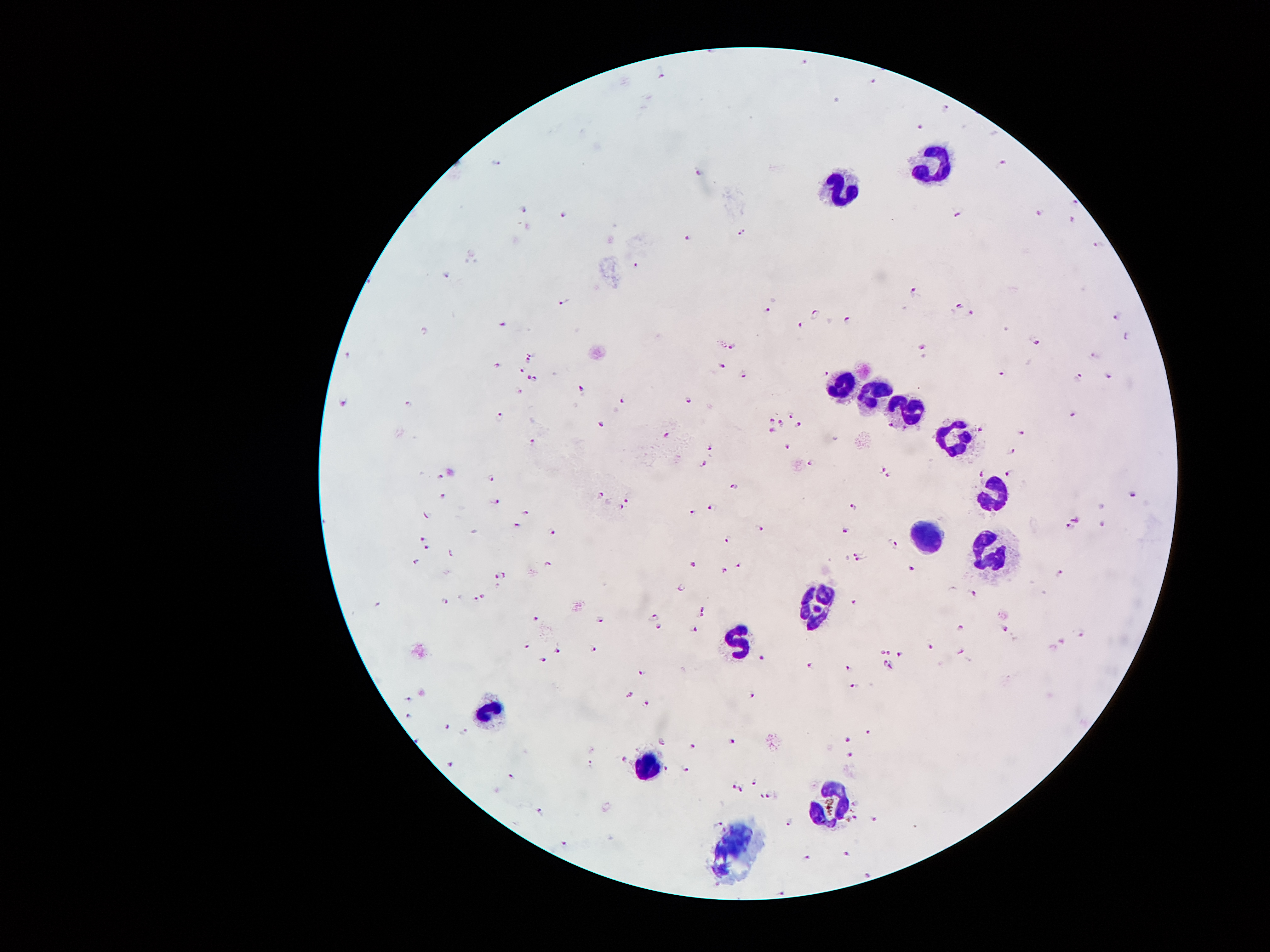
Approximate centers as [x, y] in pixels.
Summary:
  - Plasmodium parasite locations: [803, 60], [663, 76], [874, 82], [838, 98], [946, 109], [919, 126], [1002, 162], [498, 163], [698, 172], [1076, 204], [523, 208], [1038, 213], [560, 214], [957, 219], [1072, 220], [742, 232], [683, 236], [1097, 244], [635, 264], [445, 273], [509, 287], [914, 291], [562, 303], [958, 304], [766, 311], [970, 313], [815, 314], [848, 318], [1119, 318], [503, 324], [802, 325], [424, 329], [1125, 336], [1036, 341], [730, 346], [920, 346], [532, 352], [347, 355], [1096, 357], [529, 362], [494, 366], [723, 366], [522, 370], [827, 371], [1002, 373], [1079, 376], [741, 377], [529, 378], [536, 378], [1109, 378], [581, 388], [519, 390], [621, 399], [344, 401], [687, 401], [409, 403], [789, 413], [1073, 413], [500, 414], [771, 418], [780, 422], [599, 425], [797, 425], [773, 429], [980, 429], [1022, 432], [667, 435], [532, 440], [785, 446], [711, 447], [1014, 450], [701, 462], [810, 463], [882, 470], [981, 472], [438, 474], [1008, 474], [890, 476], [489, 477], [735, 485], [600, 493], [1134, 493], [442, 496], [495, 499], [626, 501], [713, 505], [620, 508], [853, 508], [691, 512], [526, 513], [427, 516], [1074, 517], [517, 524], [760, 525], [1102, 525], [1069, 528], [846, 529], [550, 530], [423, 537], [730, 539], [897, 543], [428, 546], [856, 550], [450, 554], [416, 562], [856, 562], [695, 563], [738, 563], [550, 564], [910, 567], [722, 568], [496, 573], [1061, 573], [508, 575], [680, 587], [484, 593], [974, 594], [477, 598], [445, 600], [853, 600], [378, 602], [704, 608], [702, 614], [655, 617], [537, 618], [600, 621], [695, 627], [658, 629], [962, 629], [1004, 629], [1082, 634], [1064, 639], [528, 647], [590, 648], [932, 648], [558, 650], [881, 651], [889, 651], [960, 652], [542, 657], [763, 657], [901, 657], [885, 660], [807, 664], [848, 667], [890, 668], [642, 671], [855, 685], [630, 692], [751, 696], [408, 701], [645, 706], [407, 715], [446, 726], [463, 731], [869, 731], [847, 739], [414, 740], [733, 740], [663, 743], [692, 744], [850, 753], [624, 759], [452, 762], [588, 765], [666, 768], [687, 769], [509, 773], [754, 781], [733, 783], [741, 789], [762, 797], [769, 797], [856, 802], [541, 808], [855, 816], [874, 819], [788, 822], [720, 823], [562, 841], [848, 853], [809, 856], [868, 874], [781, 891]
  - Leukocyte locations: [930, 164], [841, 189], [844, 384], [868, 396], [908, 411], [957, 438], [994, 495], [928, 539], [984, 554], [819, 604], [737, 641], [485, 707], [648, 764], [839, 806], [737, 838]
  - Patient malaria status: positive for Plasmodium falciparum
  - Field of view: single
  - Capture: smartphone through the microscope eyepiece
  - Preparation: thick blood smear
  - Image size: 1270×952 pixels
  - Magnification: 100x
  - Stain: Giemsa